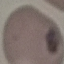
result = no malaria parasites seen
image type = automatically extracted cell patch, resized to 64 × 64 pixels
preparation = thin blood film
capture = smartphone through the microscope eyepiece
stain = Giemsa